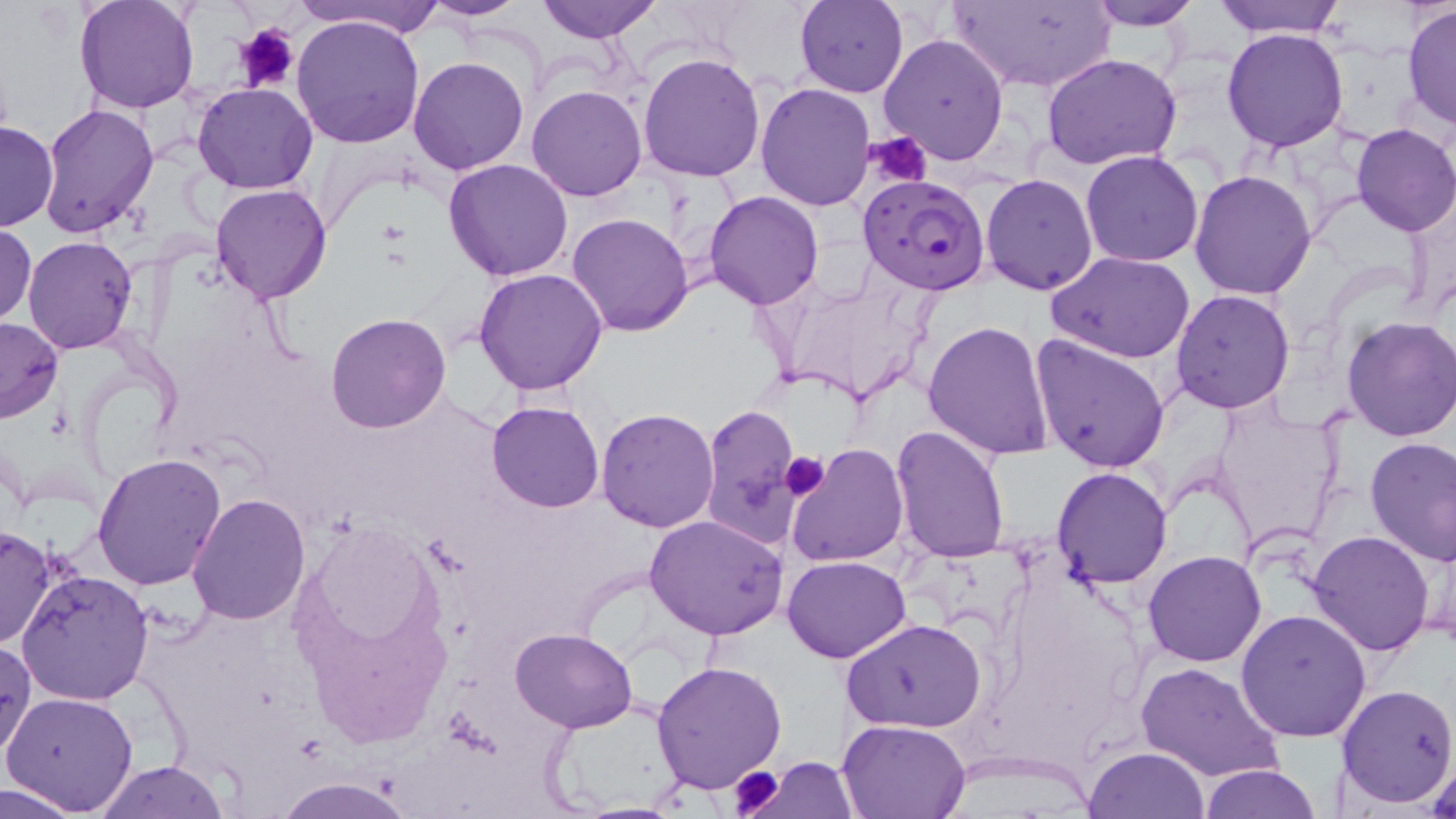
Approximate bounding boxes as [x1, y1, x2, y2] in pixels. Uninfected red blood cell locations: [74, 0, 200, 115], [290, 0, 446, 41], [422, 0, 532, 21], [537, 0, 660, 43], [795, 0, 908, 97], [1082, 0, 1200, 30], [1210, 0, 1349, 38], [946, 1, 1115, 89], [1402, 5, 1456, 134], [291, 13, 425, 150], [1221, 27, 1350, 152], [879, 33, 1009, 166], [638, 52, 766, 182], [1040, 52, 1184, 170], [408, 55, 529, 174], [193, 83, 316, 195], [754, 83, 876, 212], [527, 84, 648, 202], [38, 102, 158, 237], [1, 120, 58, 233], [1350, 123, 1456, 236], [1080, 150, 1205, 268], [442, 158, 575, 281], [1188, 168, 1319, 300], [980, 173, 1100, 295], [210, 182, 333, 304], [704, 191, 824, 310], [566, 213, 693, 336], [1, 223, 36, 327], [23, 237, 137, 354], [1048, 250, 1195, 362], [473, 268, 609, 395], [1170, 288, 1295, 413], [325, 313, 451, 433], [1340, 315, 1456, 443], [0, 316, 63, 425], [923, 318, 1055, 461], [1029, 333, 1171, 472], [1212, 400, 1345, 550], [486, 402, 604, 514], [699, 403, 804, 547], [596, 408, 721, 531], [890, 423, 1012, 563], [1364, 437, 1456, 566], [787, 444, 910, 568], [93, 454, 227, 592], [1051, 465, 1175, 588], [187, 495, 310, 625], [645, 516, 787, 641], [0, 523, 56, 650], [1308, 530, 1435, 657], [1143, 550, 1266, 667], [782, 554, 912, 662], [16, 567, 156, 706], [1235, 608, 1372, 741], [842, 618, 989, 734], [510, 627, 638, 731], [0, 634, 35, 765], [649, 660, 789, 795], [1135, 661, 1282, 785], [1335, 683, 1455, 809], [4, 690, 140, 814], [837, 717, 973, 818], [1424, 746, 1456, 818], [1084, 747, 1209, 819], [747, 758, 859, 817], [98, 760, 227, 818], [1197, 763, 1323, 819], [273, 777, 414, 818], [0, 778, 88, 817]. Plasmodium falciparum-infected red blood cell locations: [859, 174, 990, 295]. Platelet locations: [235, 22, 299, 93], [866, 131, 932, 189], [780, 452, 831, 501], [725, 766, 786, 818]. Slide-level diagnosis: Plasmodium falciparum. Light microscopy. One field of a larger specimen. 1000x magnification. Image is 1456×819 pixels. Thin blood film. May-Grünwald-Giemsa stain.